Locate every blood parasite and identify its species.
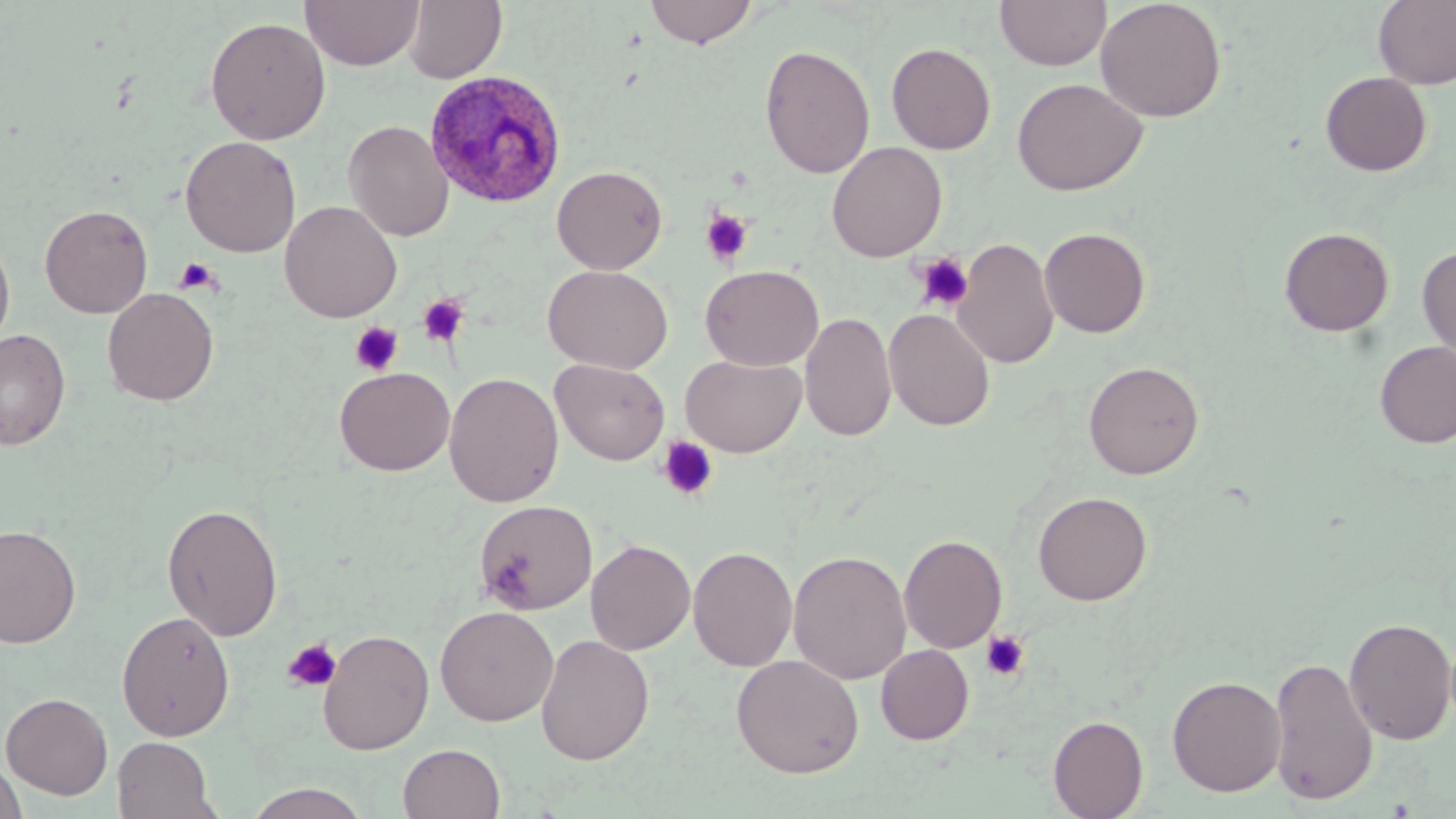

Approximate bounding boxes as named x1/y1/x2/y2 corners in pixels.
Plasmodium ovale-infected red blood cells: (x1=424, y1=69, x2=567, y2=208).
No Plasmodium falciparum, Plasmodium malariae, Plasmodium vivax, Babesia divergens, or Trypanosoma brucei observed.

slide-level diagnosis = Plasmodium ovale
uninfected red blood cell locations = approximate bounding boxes as named x1/y1/x2/y2 corners in pixels: (x1=301, y1=0, x2=424, y2=70), (x1=403, y1=0, x2=507, y2=84), (x1=644, y1=0, x2=760, y2=48), (x1=995, y1=0, x2=1110, y2=70), (x1=1095, y1=0, x2=1227, y2=122), (x1=1373, y1=0, x2=1456, y2=89), (x1=205, y1=16, x2=330, y2=145), (x1=886, y1=42, x2=996, y2=155), (x1=759, y1=44, x2=875, y2=179), (x1=1320, y1=71, x2=1432, y2=176), (x1=1011, y1=77, x2=1148, y2=196), (x1=343, y1=120, x2=453, y2=241), (x1=180, y1=135, x2=301, y2=257), (x1=826, y1=141, x2=947, y2=262), (x1=552, y1=165, x2=668, y2=274), (x1=279, y1=200, x2=402, y2=322), (x1=39, y1=204, x2=153, y2=318), (x1=1039, y1=226, x2=1151, y2=338), (x1=1279, y1=226, x2=1395, y2=337), (x1=0, y1=233, x2=15, y2=352), (x1=954, y1=237, x2=1059, y2=369), (x1=1417, y1=245, x2=1456, y2=367), (x1=543, y1=264, x2=672, y2=373), (x1=700, y1=264, x2=823, y2=370), (x1=102, y1=288, x2=219, y2=406), (x1=883, y1=308, x2=996, y2=431), (x1=800, y1=311, x2=896, y2=442), (x1=0, y1=328, x2=71, y2=450), (x1=1374, y1=340, x2=1456, y2=448), (x1=680, y1=354, x2=806, y2=457), (x1=551, y1=358, x2=669, y2=465), (x1=1083, y1=360, x2=1204, y2=479), (x1=334, y1=368, x2=454, y2=476), (x1=443, y1=372, x2=564, y2=507), (x1=1032, y1=490, x2=1152, y2=606), (x1=473, y1=499, x2=597, y2=615), (x1=161, y1=502, x2=283, y2=640), (x1=0, y1=523, x2=82, y2=649), (x1=899, y1=534, x2=1007, y2=653), (x1=585, y1=538, x2=695, y2=655), (x1=688, y1=545, x2=798, y2=672), (x1=788, y1=549, x2=912, y2=685), (x1=435, y1=606, x2=559, y2=726), (x1=117, y1=610, x2=235, y2=741), (x1=1343, y1=616, x2=1455, y2=745), (x1=317, y1=629, x2=435, y2=754), (x1=535, y1=634, x2=654, y2=765), (x1=875, y1=644, x2=974, y2=745), (x1=731, y1=654, x2=864, y2=778), (x1=1269, y1=656, x2=1377, y2=804), (x1=1166, y1=675, x2=1286, y2=797), (x1=1, y1=692, x2=114, y2=799), (x1=1048, y1=715, x2=1148, y2=819), (x1=112, y1=736, x2=220, y2=819), (x1=398, y1=742, x2=506, y2=819), (x1=0, y1=760, x2=27, y2=819), (x1=243, y1=783, x2=373, y2=819)
modality = light microscopy
preparation = thin blood film
platelet locations = approximate bounding boxes as named x1/y1/x2/y2 corners in pixels: (x1=699, y1=208, x2=755, y2=266), (x1=912, y1=252, x2=975, y2=312), (x1=174, y1=257, x2=222, y2=296), (x1=418, y1=293, x2=470, y2=347), (x1=350, y1=321, x2=403, y2=375), (x1=657, y1=436, x2=719, y2=501), (x1=980, y1=630, x2=1030, y2=681), (x1=282, y1=637, x2=343, y2=693)
magnification = 1000x
field of view = single
stain = May-Grünwald-Giemsa
image size = 1456×819 pixels